Identify the blood parasite species.
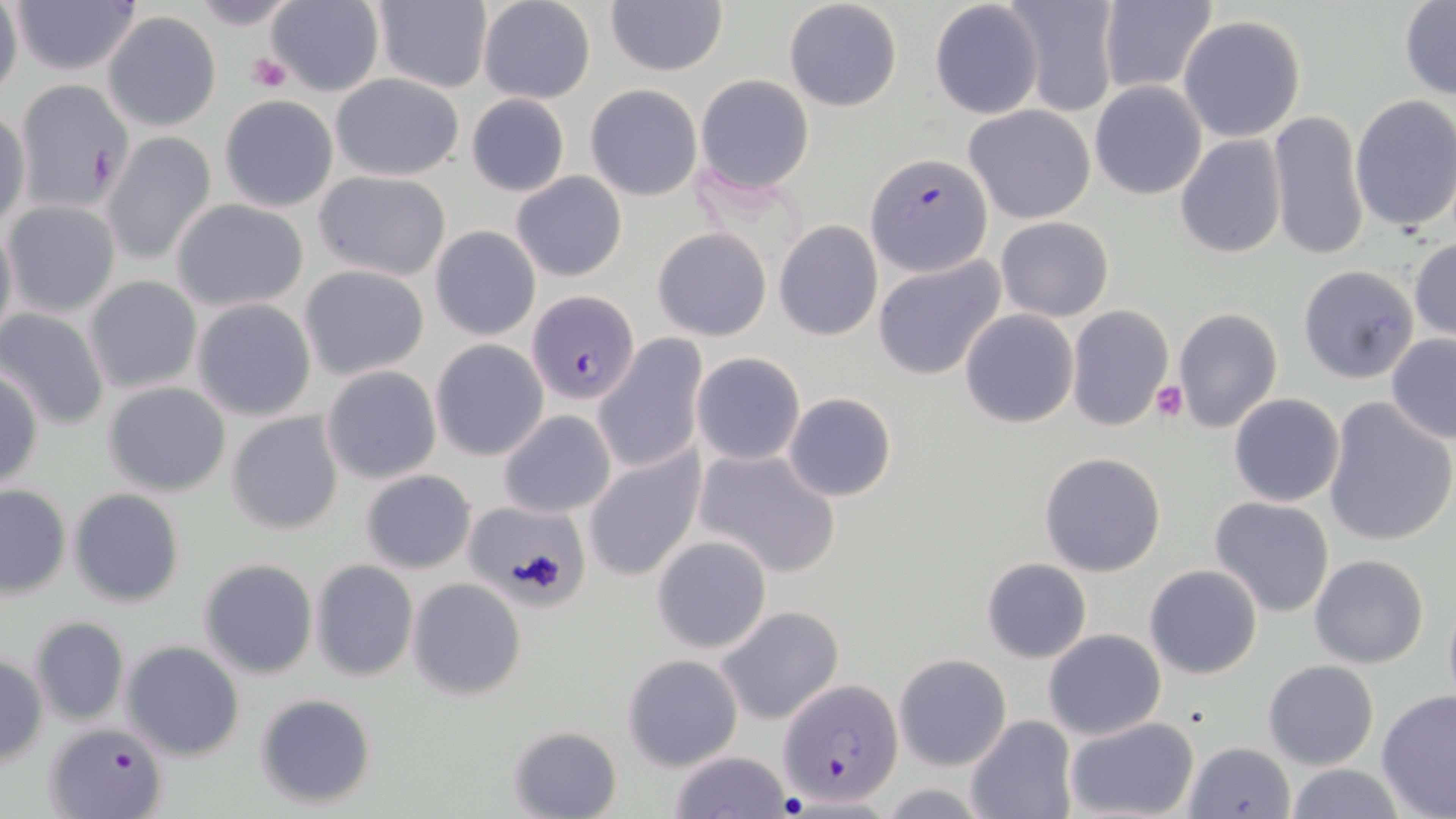

Plasmodium falciparum.

Approximate bounding boxes as named x1/y1/x2/y2 corners in pixels. Platelet locations: (x1=246, y1=51, x2=292, y2=93), (x1=1151, y1=382, x2=1189, y2=422). Plasmodium falciparum-infected red blood cell locations: (x1=866, y1=151, x2=994, y2=277), (x1=527, y1=290, x2=639, y2=405), (x1=780, y1=679, x2=902, y2=806), (x1=46, y1=720, x2=168, y2=817). Uninfected red blood cell locations: (x1=0, y1=0, x2=23, y2=103), (x1=8, y1=0, x2=144, y2=77), (x1=187, y1=0, x2=304, y2=30), (x1=370, y1=0, x2=493, y2=94), (x1=477, y1=0, x2=597, y2=105), (x1=605, y1=0, x2=727, y2=77), (x1=783, y1=0, x2=904, y2=114), (x1=266, y1=1, x2=384, y2=96), (x1=1096, y1=1, x2=1218, y2=95), (x1=1398, y1=1, x2=1455, y2=101), (x1=929, y1=2, x2=1043, y2=119), (x1=1004, y1=2, x2=1119, y2=115), (x1=105, y1=13, x2=221, y2=131), (x1=1178, y1=15, x2=1307, y2=142), (x1=330, y1=72, x2=467, y2=182), (x1=695, y1=74, x2=815, y2=193), (x1=12, y1=78, x2=135, y2=213), (x1=1089, y1=80, x2=1207, y2=200), (x1=585, y1=84, x2=701, y2=201), (x1=466, y1=93, x2=570, y2=197), (x1=218, y1=95, x2=339, y2=212), (x1=1350, y1=95, x2=1456, y2=234), (x1=962, y1=103, x2=1096, y2=223), (x1=1, y1=109, x2=30, y2=229), (x1=1268, y1=109, x2=1369, y2=264), (x1=102, y1=128, x2=216, y2=261), (x1=1175, y1=136, x2=1286, y2=259), (x1=313, y1=171, x2=452, y2=280), (x1=510, y1=172, x2=628, y2=282), (x1=170, y1=199, x2=310, y2=311), (x1=4, y1=200, x2=121, y2=319), (x1=0, y1=215, x2=17, y2=349), (x1=995, y1=215, x2=1114, y2=322), (x1=773, y1=220, x2=884, y2=339), (x1=430, y1=225, x2=541, y2=341), (x1=653, y1=227, x2=771, y2=342), (x1=1409, y1=235, x2=1456, y2=343), (x1=871, y1=256, x2=1006, y2=381), (x1=298, y1=263, x2=430, y2=382), (x1=1297, y1=265, x2=1419, y2=384), (x1=83, y1=274, x2=202, y2=394), (x1=191, y1=297, x2=318, y2=422), (x1=1066, y1=305, x2=1174, y2=431), (x1=0, y1=306, x2=110, y2=430), (x1=959, y1=308, x2=1079, y2=429), (x1=1172, y1=308, x2=1282, y2=432), (x1=1386, y1=333, x2=1456, y2=444), (x1=593, y1=335, x2=706, y2=473), (x1=429, y1=338, x2=549, y2=462), (x1=691, y1=352, x2=806, y2=466), (x1=0, y1=365, x2=44, y2=490), (x1=321, y1=365, x2=442, y2=485), (x1=102, y1=381, x2=231, y2=497), (x1=783, y1=392, x2=897, y2=502), (x1=1229, y1=393, x2=1344, y2=506), (x1=1323, y1=398, x2=1456, y2=548), (x1=226, y1=409, x2=345, y2=536), (x1=498, y1=409, x2=616, y2=519), (x1=583, y1=447, x2=707, y2=582), (x1=694, y1=447, x2=843, y2=578), (x1=1039, y1=452, x2=1167, y2=576), (x1=360, y1=469, x2=476, y2=573), (x1=0, y1=484, x2=71, y2=597), (x1=69, y1=489, x2=185, y2=608), (x1=1208, y1=497, x2=1335, y2=619), (x1=463, y1=500, x2=590, y2=610), (x1=652, y1=535, x2=772, y2=653), (x1=1309, y1=553, x2=1430, y2=670), (x1=198, y1=557, x2=319, y2=680), (x1=981, y1=557, x2=1092, y2=663), (x1=310, y1=559, x2=419, y2=682), (x1=1144, y1=565, x2=1263, y2=680), (x1=407, y1=578, x2=526, y2=700), (x1=1442, y1=589, x2=1456, y2=711), (x1=716, y1=605, x2=844, y2=725), (x1=30, y1=616, x2=129, y2=725), (x1=1042, y1=629, x2=1166, y2=740), (x1=114, y1=647, x2=239, y2=769), (x1=622, y1=653, x2=742, y2=770), (x1=894, y1=653, x2=1012, y2=772), (x1=0, y1=654, x2=47, y2=765), (x1=1262, y1=660, x2=1379, y2=769), (x1=1376, y1=689, x2=1456, y2=818), (x1=253, y1=691, x2=377, y2=810), (x1=964, y1=715, x2=1078, y2=819), (x1=1063, y1=716, x2=1199, y2=819), (x1=507, y1=724, x2=622, y2=819), (x1=1182, y1=740, x2=1298, y2=819), (x1=666, y1=750, x2=791, y2=818), (x1=1285, y1=763, x2=1406, y2=819). 1000x magnification. May-Grünwald-Giemsa stain. Thin blood smear. Single field of view. Image is 1456×819 pixels. Light microscopy.